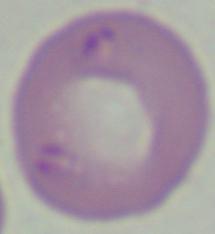
Summary:
  - Magnification: 1000x
  - Identification: Babesia
  - Modality: micrograph